Assess this cell for malaria.
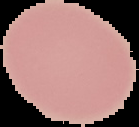

Uninfected.

Summary:
  - Image size: 139×127 pixels
  - Preparation: thin blood film
  - Image type: segmented cell region on a black background